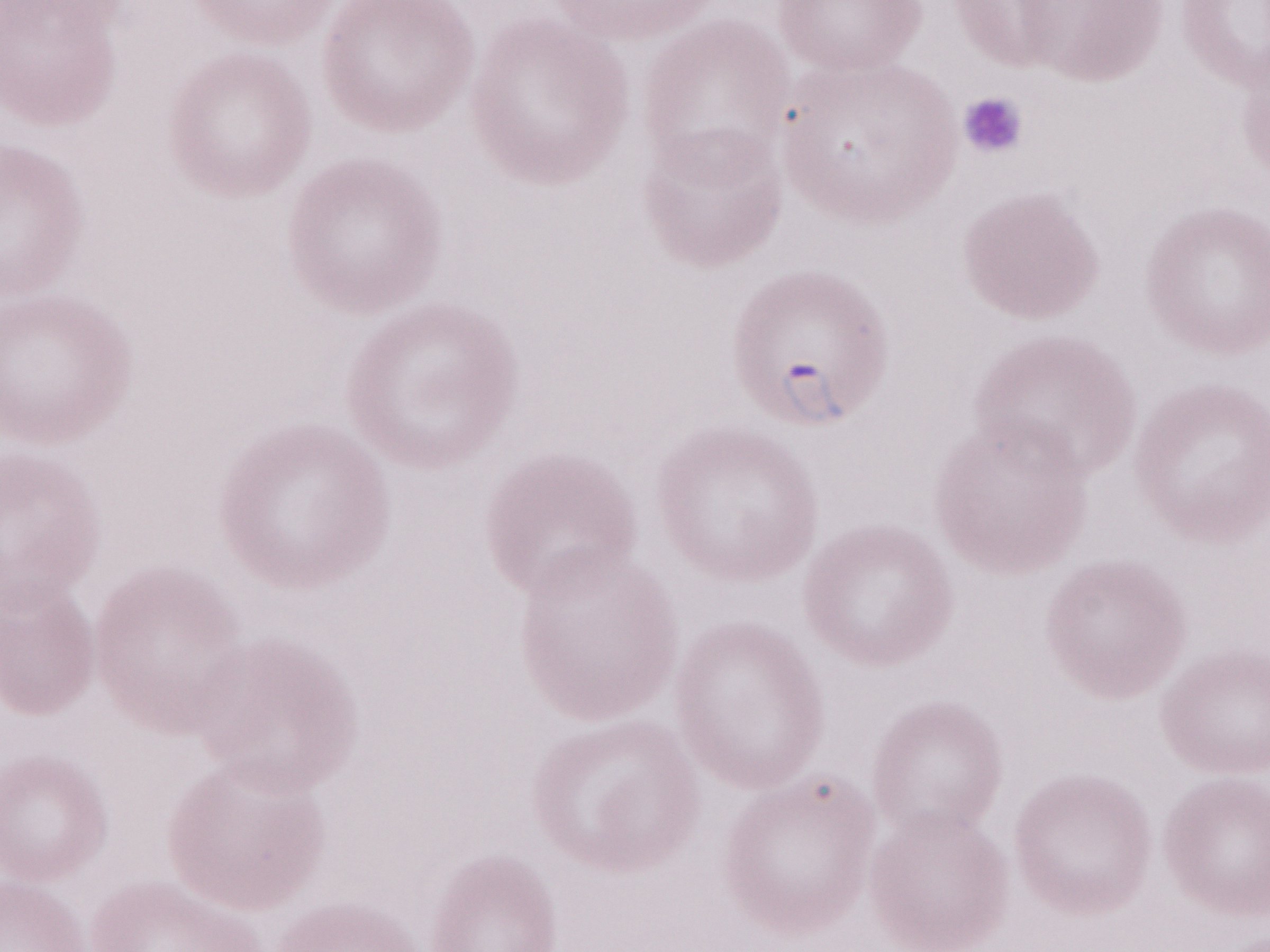

Single field of view. Patient diagnosis: malaria infection. Image is 1270×952 pixels. May-Grünwald-Giemsa stain. Olympus BX43 microscope and DP73 digital camera. Thin blood smear. Magnification: 1,000x.